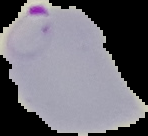
From a thin blood smear. Image is 148×136 pixels. The area outside the segmented cell region is set to black. Malaria status: parasitized.